Locate and identify every blood parasite.
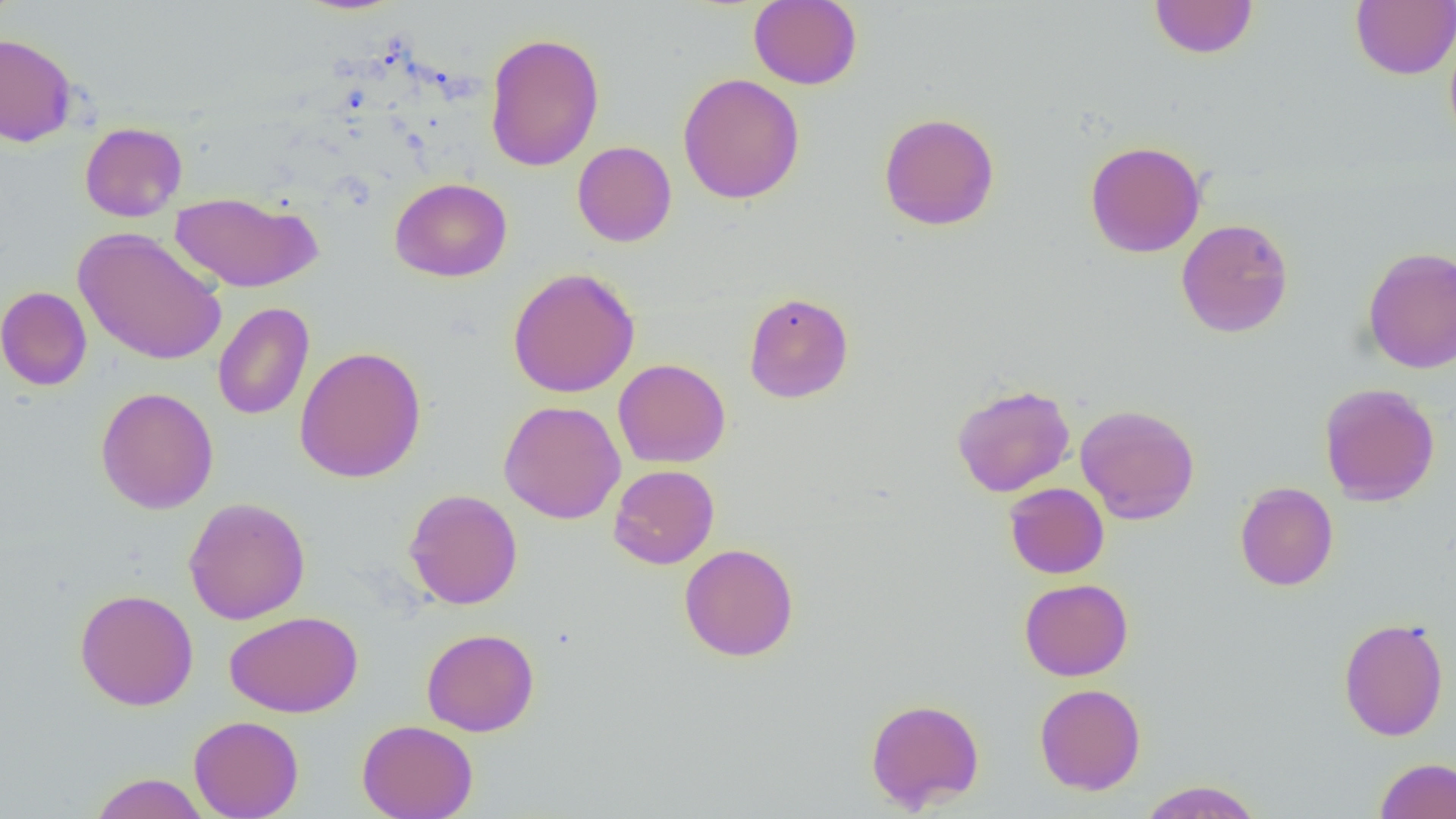

No blood parasites seen.

Summary:
  - Coordinate format: approximate bounding boxes as [x1, y1, x2, y2] in pixels
  - Uninfected red blood cell locations: [0, 0, 23, 25], [748, 0, 862, 89], [1351, 0, 1456, 80], [1149, 1, 1258, 59], [1444, 26, 1456, 149], [484, 32, 604, 172], [0, 33, 78, 147], [677, 73, 805, 204], [878, 112, 1000, 231], [79, 121, 187, 222], [1084, 140, 1206, 258], [572, 141, 677, 247], [390, 178, 512, 282], [170, 191, 323, 293], [1175, 218, 1293, 337], [73, 227, 228, 366], [1362, 246, 1456, 374], [507, 267, 640, 398], [0, 286, 92, 391], [743, 292, 854, 403], [212, 302, 314, 421], [294, 346, 427, 483], [613, 358, 731, 468], [1319, 382, 1440, 506], [951, 383, 1075, 497], [95, 387, 219, 514], [498, 400, 626, 524], [1075, 404, 1200, 524], [608, 464, 719, 569], [1004, 482, 1109, 578], [1235, 482, 1339, 591], [1012, 483, 1116, 680], [403, 488, 523, 610], [183, 496, 311, 624], [679, 543, 799, 662], [1019, 578, 1133, 681], [74, 588, 199, 710], [224, 611, 363, 718], [1338, 616, 1450, 742], [421, 628, 540, 737], [1034, 683, 1146, 795], [865, 697, 985, 812], [189, 715, 304, 818], [357, 719, 478, 819], [1374, 757, 1456, 818], [89, 772, 210, 818], [1138, 780, 1264, 818]
  - Slide-level diagnosis: no evidence of blood parasites
  - Field of view: one of a larger specimen
  - Magnification: 1000x
  - Modality: optical microscopy
  - Preparation: thin blood smear
  - Image size: 1456×819 pixels